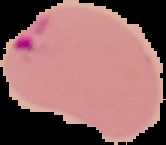
Summary:
  - Image type: segmented cell region with the area outside set to black
  - Preparation: thin blood smear
  - Image size: 166×145 pixels
  - Malaria status: parasitized